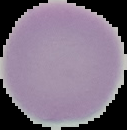 Malaria status: uninfected. From a thin blood film. The area outside the segmented cell region is set to black. Image is 127×130 pixels.